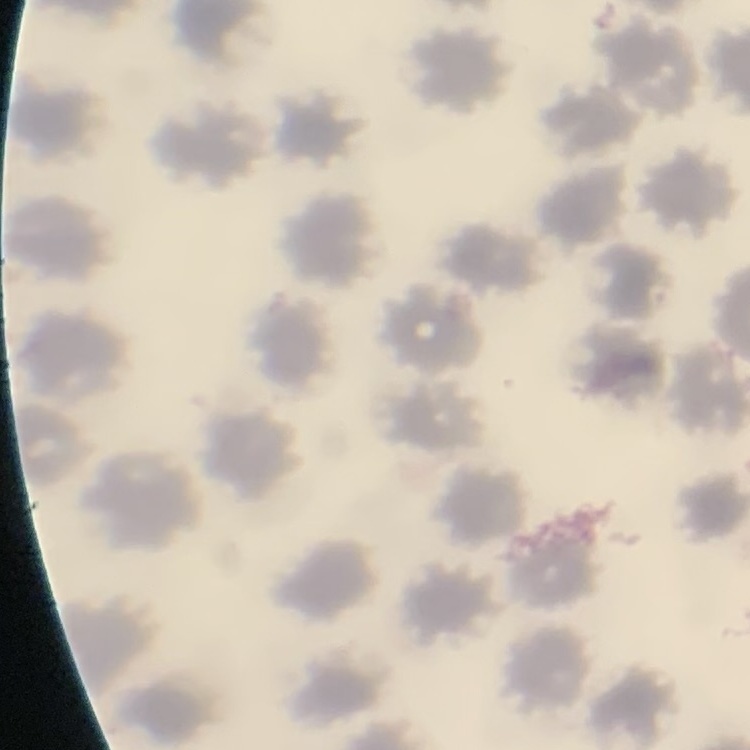

Summary:
  - Erythrocyte morphology: no rouleaux formation
  - Image type: square crop of a larger photomicrograph
  - Preparation: thin blood film
  - Stain: Field's or Giemsa